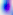
Photomicrograph. Toxoplasma gondii is seen. 400x magnification.